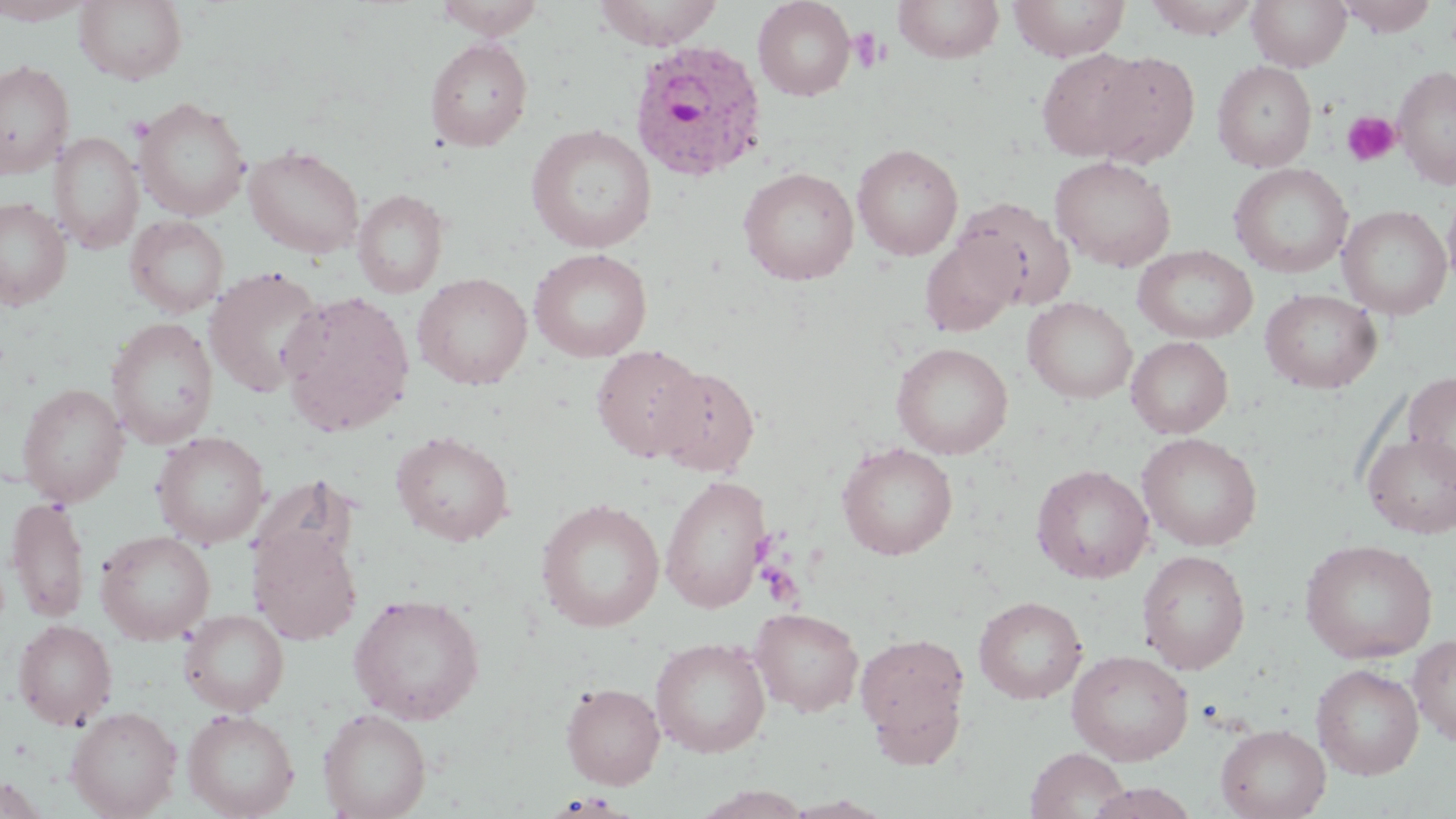 Approximate bounding boxes as named x1/y1/x2/y2 corners in pixels. Plasmodium ovale-infected red blood cell locations: (x1=628, y1=40, x2=768, y2=182). Uninfected red blood cell locations: (x1=0, y1=0, x2=95, y2=25), (x1=74, y1=0, x2=188, y2=85), (x1=432, y1=0, x2=547, y2=38), (x1=591, y1=0, x2=726, y2=49), (x1=752, y1=0, x2=857, y2=101), (x1=893, y1=0, x2=1005, y2=64), (x1=1008, y1=0, x2=1130, y2=61), (x1=1143, y1=0, x2=1260, y2=39), (x1=1247, y1=0, x2=1351, y2=72), (x1=1338, y1=0, x2=1438, y2=37), (x1=425, y1=38, x2=533, y2=152), (x1=1036, y1=48, x2=1152, y2=162), (x1=1085, y1=50, x2=1200, y2=167), (x1=0, y1=59, x2=74, y2=178), (x1=1212, y1=61, x2=1317, y2=172), (x1=1393, y1=65, x2=1456, y2=190), (x1=134, y1=96, x2=252, y2=221), (x1=526, y1=125, x2=657, y2=252), (x1=50, y1=130, x2=144, y2=254), (x1=852, y1=143, x2=963, y2=260), (x1=243, y1=144, x2=365, y2=259), (x1=1049, y1=156, x2=1176, y2=271), (x1=1229, y1=163, x2=1353, y2=279), (x1=738, y1=166, x2=859, y2=285), (x1=1442, y1=182, x2=1456, y2=295), (x1=352, y1=189, x2=449, y2=299), (x1=954, y1=196, x2=1076, y2=310), (x1=0, y1=197, x2=71, y2=310), (x1=1337, y1=205, x2=1453, y2=319), (x1=126, y1=215, x2=229, y2=319), (x1=919, y1=235, x2=1021, y2=337), (x1=1133, y1=245, x2=1258, y2=344), (x1=529, y1=248, x2=652, y2=362), (x1=203, y1=266, x2=326, y2=397), (x1=413, y1=273, x2=533, y2=390), (x1=1259, y1=289, x2=1382, y2=393), (x1=278, y1=290, x2=415, y2=436), (x1=1023, y1=297, x2=1137, y2=403), (x1=106, y1=317, x2=219, y2=449), (x1=1126, y1=336, x2=1233, y2=438), (x1=891, y1=342, x2=1014, y2=459), (x1=591, y1=344, x2=705, y2=461), (x1=653, y1=365, x2=760, y2=476), (x1=1403, y1=371, x2=1456, y2=482), (x1=18, y1=383, x2=129, y2=505), (x1=151, y1=431, x2=270, y2=548), (x1=391, y1=431, x2=515, y2=545), (x1=1362, y1=432, x2=1456, y2=538), (x1=1137, y1=433, x2=1263, y2=552), (x1=837, y1=442, x2=958, y2=560), (x1=1031, y1=464, x2=1154, y2=583), (x1=660, y1=474, x2=771, y2=613), (x1=249, y1=477, x2=357, y2=579), (x1=6, y1=495, x2=91, y2=623), (x1=535, y1=498, x2=666, y2=632), (x1=248, y1=526, x2=362, y2=645), (x1=96, y1=530, x2=215, y2=644), (x1=1299, y1=538, x2=1439, y2=663), (x1=1137, y1=550, x2=1252, y2=674), (x1=349, y1=593, x2=486, y2=725), (x1=973, y1=596, x2=1087, y2=704), (x1=749, y1=607, x2=864, y2=716), (x1=179, y1=609, x2=289, y2=715), (x1=12, y1=619, x2=117, y2=730), (x1=855, y1=632, x2=971, y2=759), (x1=1409, y1=635, x2=1456, y2=746), (x1=650, y1=637, x2=770, y2=757), (x1=1067, y1=649, x2=1194, y2=765), (x1=1312, y1=663, x2=1424, y2=780), (x1=561, y1=682, x2=665, y2=789), (x1=66, y1=706, x2=182, y2=818), (x1=182, y1=708, x2=299, y2=819), (x1=318, y1=708, x2=432, y2=819), (x1=1216, y1=724, x2=1331, y2=819), (x1=1025, y1=746, x2=1130, y2=819), (x1=0, y1=774, x2=51, y2=818), (x1=1085, y1=782, x2=1200, y2=819), (x1=693, y1=785, x2=813, y2=819), (x1=780, y1=796, x2=895, y2=818). Platelet locations: (x1=850, y1=29, x2=887, y2=74), (x1=1341, y1=110, x2=1401, y2=167), (x1=758, y1=562, x2=803, y2=607). Slide-level diagnosis: Plasmodium ovale. 1000x magnification. Light microscopy. May-Grünwald-Giemsa-stained preparation. Thin blood smear. Single field of view. Image is 1456×819 pixels.